Identify the cell.
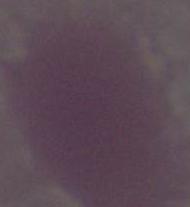

An erythrocyte.

1000x magnification. Photomicrograph.